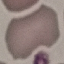
Malaria status: uninfected. Cell patch, automatically extracted from a larger field of view and resized to 64 × 64 pixels. Acquired by smartphone through the microscope eyepiece. Giemsa-stained preparation. Thin blood smear.